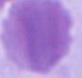
Summary:
  - Magnification: 1000x
  - Modality: micrograph
  - Identification: red blood cell